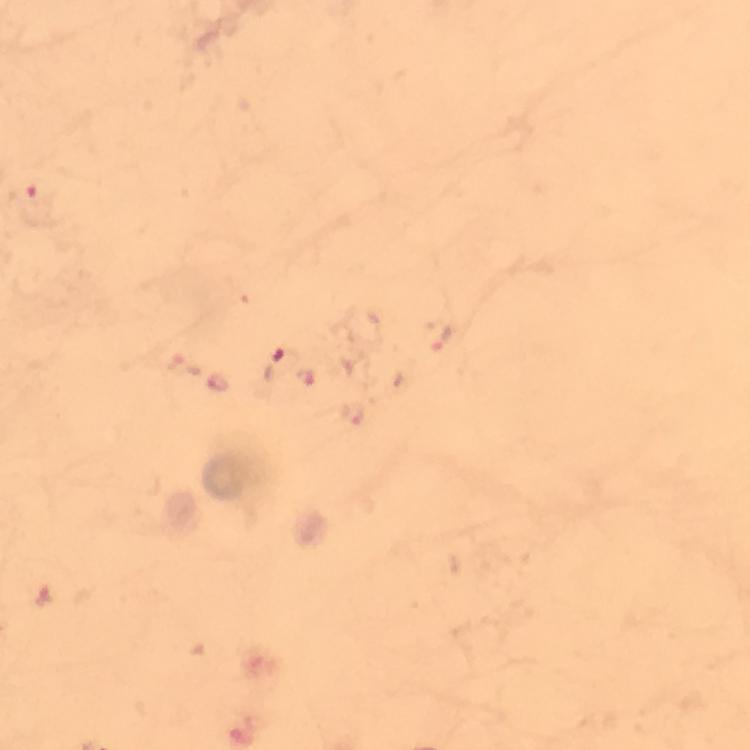
preparation: thick blood smear
plasmodium_parasite_locations: 'approximate centers as {x, y} in pixels: {34, 193}, {283, 362}'
stain: Giemsa
cropped_from: a single field of view
magnification: 100x
image_size: 750×750 pixels
capture: smartphone photograph through a microscope
context: from a malaria diagnostic workup
immersion_oil: used